Comment on the morphology of the erythrocytes.
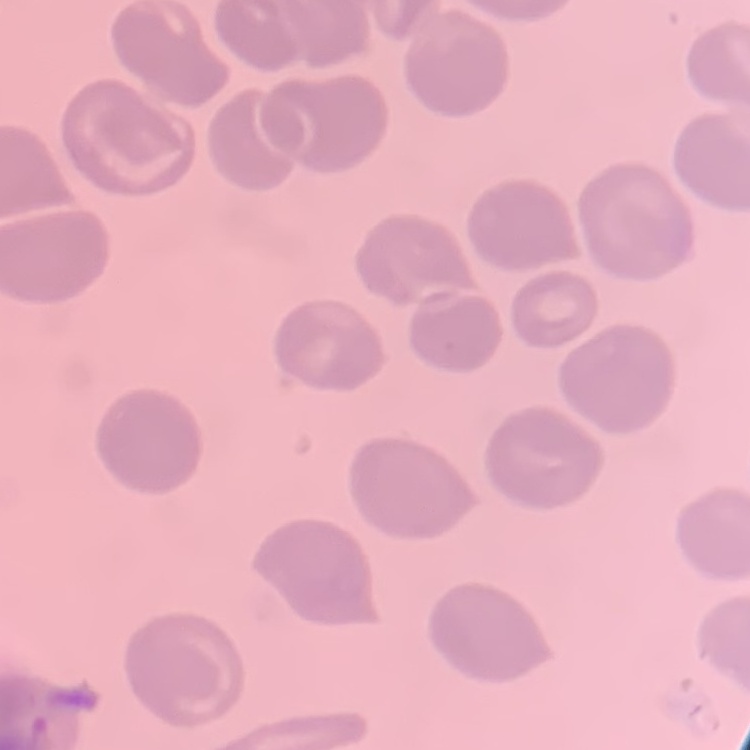
No rouleaux formation.

Summary:
  - Stain: Field's or Giemsa
  - Preparation: thin peripheral smear
  - Image type: square crop of a larger photomicrograph